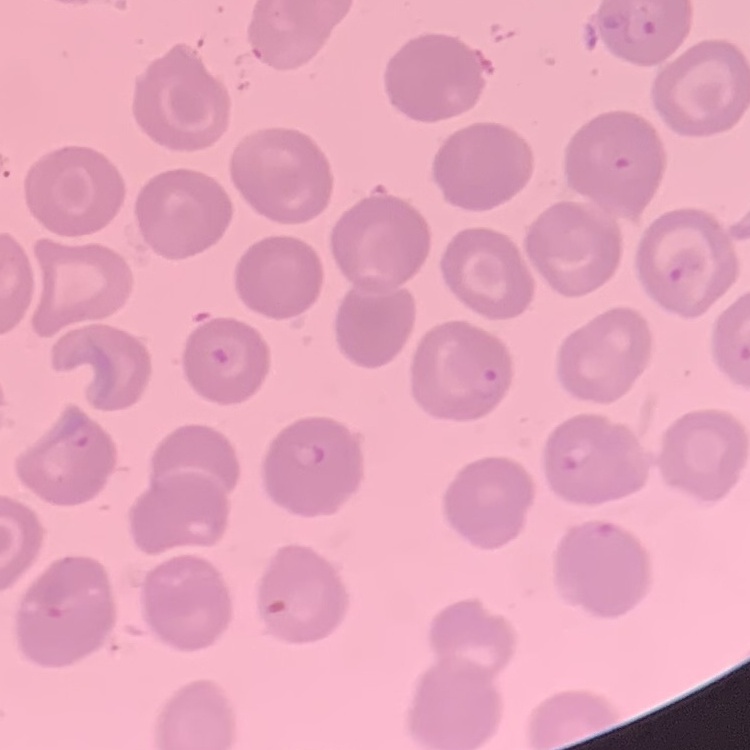 The erythrocytes exhibit no rouleaux formation. Field's or Giemsa stain. Thin blood smear. One tile cut from a larger photomicrograph.